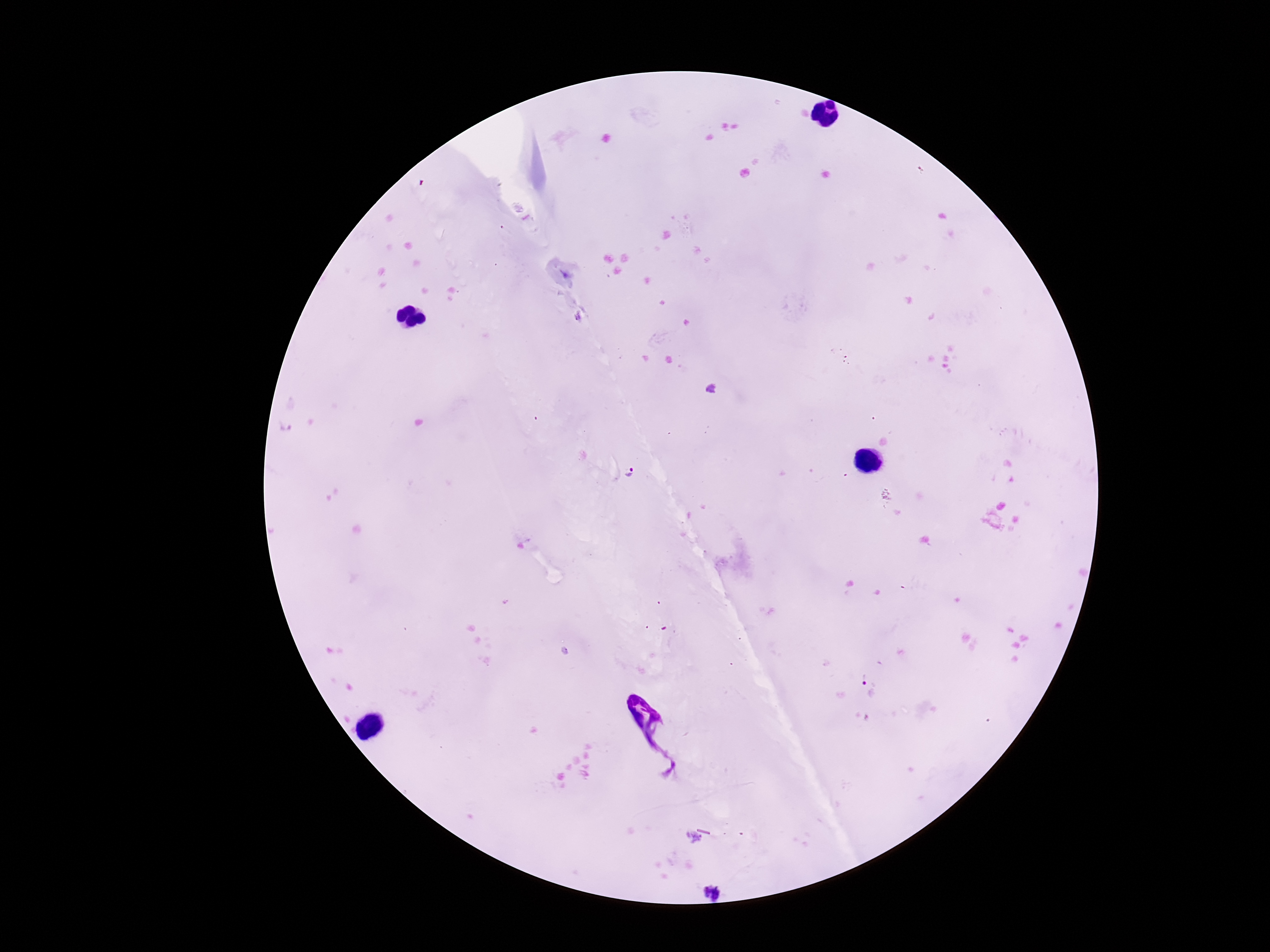

stain = Giemsa
magnification = 100x
capture = smartphone camera through the microscope eyepiece
patient malaria status = positive
image size = 1270×952 pixels
preparation = thick peripheral-blood smear
field of view = one from this slide
Plasmodium parasite locations = approximate centers as (x, y) in pixels: (632, 473), (861, 676), (711, 891)